Classify this cell by malaria status.
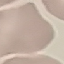
Uninfected.

Summary:
  - Stain: Giemsa
  - Image type: automatically extracted cell patch, resized to 64 × 64 pixels
  - Preparation: thin smear
  - Capture: smartphone through the microscope eyepiece